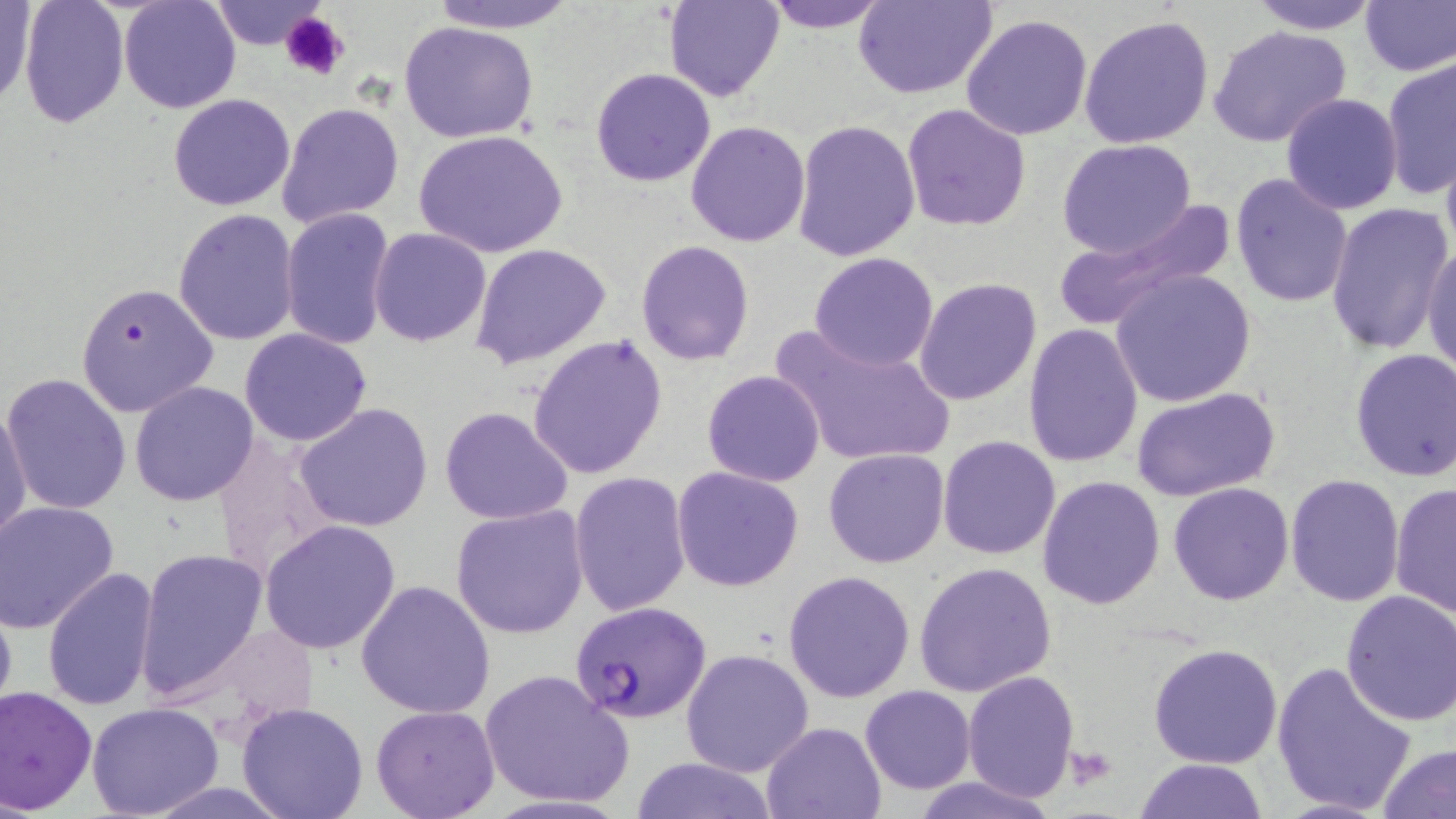
Summary:
  - Coordinate format: approximate bounding boxes as [x1, y1, x2, y2] in pixels
  - Plasmodium falciparum-infected red blood cell locations: [571, 599, 712, 723]
  - Platelet locations: [280, 13, 350, 82], [1068, 746, 1116, 789]
  - Uninfected red blood cell locations: [1, 0, 34, 106], [16, 0, 131, 129], [118, 0, 241, 114], [424, 0, 583, 32], [662, 0, 784, 103], [756, 0, 894, 32], [855, 0, 998, 99], [1243, 0, 1383, 35], [1357, 0, 1456, 75], [209, 1, 329, 50], [961, 13, 1093, 140], [1079, 14, 1213, 148], [399, 20, 539, 144], [1209, 26, 1352, 148], [1380, 55, 1456, 200], [590, 68, 716, 187], [1280, 93, 1403, 214], [167, 94, 295, 210], [276, 102, 403, 230], [902, 102, 1032, 231], [686, 119, 812, 247], [792, 119, 920, 261], [414, 129, 568, 257], [1057, 138, 1198, 259], [1440, 147, 1456, 269], [1230, 172, 1355, 307], [1053, 200, 1239, 334], [1323, 201, 1454, 356], [173, 208, 301, 344], [279, 208, 396, 350], [370, 229, 492, 346], [1423, 240, 1455, 381], [635, 241, 755, 366], [470, 242, 613, 371], [809, 253, 938, 370], [1111, 270, 1255, 407], [915, 278, 1041, 405], [74, 280, 220, 418], [1022, 324, 1144, 468], [771, 326, 957, 468], [239, 328, 372, 446], [526, 334, 668, 479], [1349, 348, 1456, 483], [702, 370, 824, 488], [2, 372, 131, 516], [129, 381, 259, 505], [1131, 386, 1281, 502], [293, 402, 434, 532], [1, 403, 33, 545], [440, 407, 573, 525], [214, 434, 340, 579], [938, 435, 1061, 560], [825, 448, 948, 569], [671, 465, 804, 591], [569, 470, 692, 616], [1284, 473, 1403, 609], [1037, 477, 1166, 609], [1167, 482, 1294, 605], [1389, 482, 1456, 619], [1, 501, 120, 634], [449, 504, 590, 637], [258, 518, 402, 655], [135, 547, 268, 701], [914, 562, 1055, 695], [43, 568, 161, 712], [783, 570, 916, 703], [356, 580, 495, 720], [0, 590, 17, 729], [1338, 591, 1456, 726], [1149, 641, 1283, 769], [682, 647, 814, 777], [1271, 660, 1418, 813], [480, 669, 634, 809], [965, 671, 1082, 799], [859, 685, 977, 796], [0, 686, 99, 814], [235, 701, 369, 819], [86, 702, 225, 819], [372, 703, 498, 819], [760, 720, 887, 819], [1378, 743, 1456, 818], [623, 757, 783, 818], [1135, 758, 1267, 819]
  - Slide-level diagnosis: Plasmodium falciparum
  - Modality: optical microscopy
  - Preparation: thin blood smear
  - Field of view: single
  - Magnification: 1000x
  - Stain: May-Grünwald-Giemsa
  - Image size: 1456×819 pixels